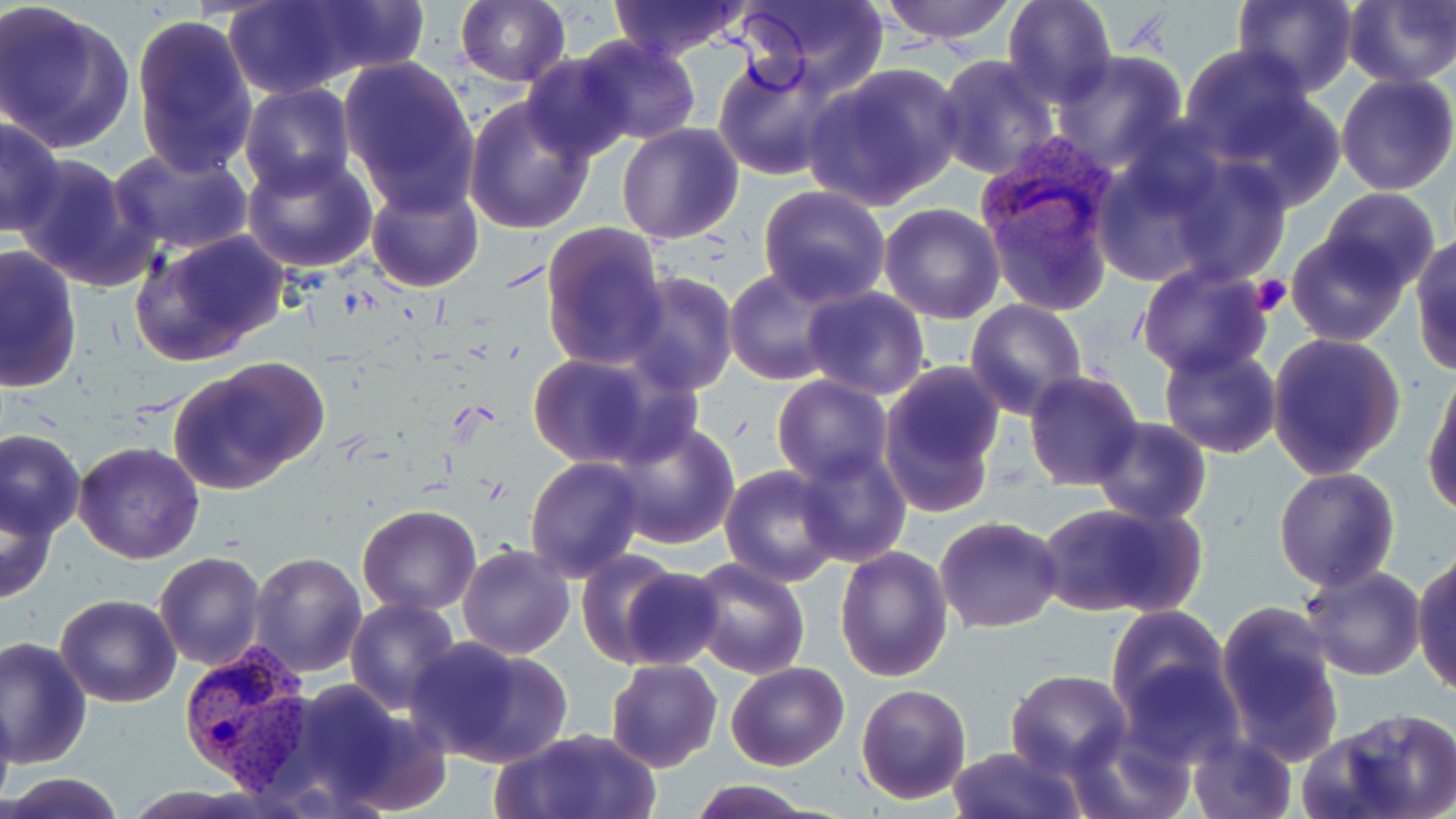

slide-level diagnosis = Plasmodium vivax
field of view = single
preparation = thin blood smear
stain = May-Grünwald-Giemsa
platelet locations = approximate bounding boxes as named x1/y1/x2/y2 corners in pixels: (x1=1251, y1=274, x2=1291, y2=316)
uninfected red blood cell locations = approximate bounding boxes as named x1/y1/x2/y2 corners in pixels: (x1=222, y1=0, x2=368, y2=99), (x1=283, y1=0, x2=430, y2=83), (x1=607, y1=0, x2=750, y2=60), (x1=736, y1=0, x2=889, y2=96), (x1=879, y1=0, x2=1020, y2=44), (x1=1003, y1=0, x2=1117, y2=107), (x1=1232, y1=0, x2=1359, y2=93), (x1=0, y1=1, x2=136, y2=154), (x1=455, y1=1, x2=570, y2=87), (x1=1343, y1=1, x2=1456, y2=87), (x1=130, y1=15, x2=258, y2=173), (x1=574, y1=36, x2=704, y2=146), (x1=1176, y1=44, x2=1315, y2=161), (x1=1049, y1=51, x2=1190, y2=169), (x1=521, y1=52, x2=635, y2=163), (x1=933, y1=53, x2=1060, y2=180), (x1=337, y1=55, x2=480, y2=207), (x1=713, y1=56, x2=844, y2=181), (x1=802, y1=63, x2=965, y2=209), (x1=1335, y1=72, x2=1456, y2=194), (x1=239, y1=84, x2=356, y2=196), (x1=1208, y1=87, x2=1348, y2=209), (x1=464, y1=94, x2=596, y2=233), (x1=1, y1=117, x2=66, y2=236), (x1=616, y1=122, x2=745, y2=244), (x1=108, y1=145, x2=255, y2=257), (x1=10, y1=151, x2=159, y2=293), (x1=241, y1=153, x2=379, y2=274), (x1=1086, y1=155, x2=1220, y2=286), (x1=1165, y1=157, x2=1290, y2=284), (x1=366, y1=182, x2=484, y2=293), (x1=759, y1=185, x2=890, y2=307), (x1=1319, y1=188, x2=1441, y2=294), (x1=877, y1=202, x2=1005, y2=323), (x1=540, y1=222, x2=668, y2=369), (x1=129, y1=229, x2=291, y2=367), (x1=1286, y1=230, x2=1410, y2=346), (x1=1411, y1=235, x2=1456, y2=373), (x1=0, y1=245, x2=82, y2=392), (x1=1135, y1=262, x2=1270, y2=378), (x1=725, y1=269, x2=844, y2=384), (x1=620, y1=272, x2=739, y2=396), (x1=799, y1=288, x2=931, y2=401), (x1=964, y1=300, x2=1087, y2=420), (x1=1266, y1=332, x2=1405, y2=479), (x1=1157, y1=342, x2=1285, y2=459), (x1=523, y1=352, x2=689, y2=471), (x1=168, y1=358, x2=330, y2=494), (x1=878, y1=362, x2=1005, y2=513), (x1=1023, y1=370, x2=1146, y2=492), (x1=1422, y1=370, x2=1455, y2=519), (x1=771, y1=376, x2=894, y2=486), (x1=1090, y1=417, x2=1211, y2=525), (x1=605, y1=420, x2=740, y2=550), (x1=1, y1=430, x2=85, y2=539), (x1=72, y1=442, x2=205, y2=565), (x1=792, y1=446, x2=912, y2=568), (x1=524, y1=456, x2=646, y2=582), (x1=720, y1=466, x2=844, y2=586), (x1=1274, y1=467, x2=1399, y2=591), (x1=2, y1=493, x2=60, y2=606), (x1=1034, y1=498, x2=1205, y2=621), (x1=357, y1=503, x2=481, y2=615), (x1=935, y1=515, x2=1065, y2=634), (x1=457, y1=544, x2=574, y2=659), (x1=835, y1=546, x2=955, y2=684), (x1=574, y1=549, x2=685, y2=668), (x1=1411, y1=549, x2=1456, y2=697), (x1=249, y1=551, x2=367, y2=677), (x1=153, y1=552, x2=266, y2=670), (x1=687, y1=557, x2=812, y2=679), (x1=1298, y1=564, x2=1427, y2=681), (x1=610, y1=566, x2=728, y2=671), (x1=55, y1=595, x2=182, y2=708), (x1=346, y1=599, x2=461, y2=715), (x1=1214, y1=601, x2=1346, y2=765), (x1=1106, y1=605, x2=1230, y2=722), (x1=1, y1=635, x2=92, y2=771), (x1=405, y1=635, x2=573, y2=769), (x1=1115, y1=655, x2=1243, y2=768), (x1=605, y1=657, x2=722, y2=771), (x1=725, y1=661, x2=849, y2=769), (x1=1005, y1=670, x2=1131, y2=778), (x1=244, y1=675, x2=449, y2=813), (x1=856, y1=682, x2=972, y2=804), (x1=0, y1=692, x2=18, y2=810), (x1=1313, y1=706, x2=1456, y2=819), (x1=1064, y1=720, x2=1193, y2=819), (x1=494, y1=728, x2=660, y2=819), (x1=1187, y1=735, x2=1296, y2=818), (x1=946, y1=745, x2=1085, y2=819), (x1=4, y1=770, x2=125, y2=818), (x1=687, y1=781, x2=820, y2=818)
Plasmodium vivax-infected red blood cell locations = approximate bounding boxes as named x1/y1/x2/y2 corners in pixels: (x1=974, y1=138, x2=1122, y2=267), (x1=180, y1=640, x2=314, y2=789)
image size = 1456×819 pixels
modality = optical microscopy
magnification = 1000x